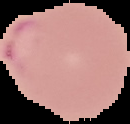

Cell region segmented out of the field of view; the surrounding area is masked to black. From a thin blood film. Image is 130×124 pixels. Result: Plasmodium parasites detected.